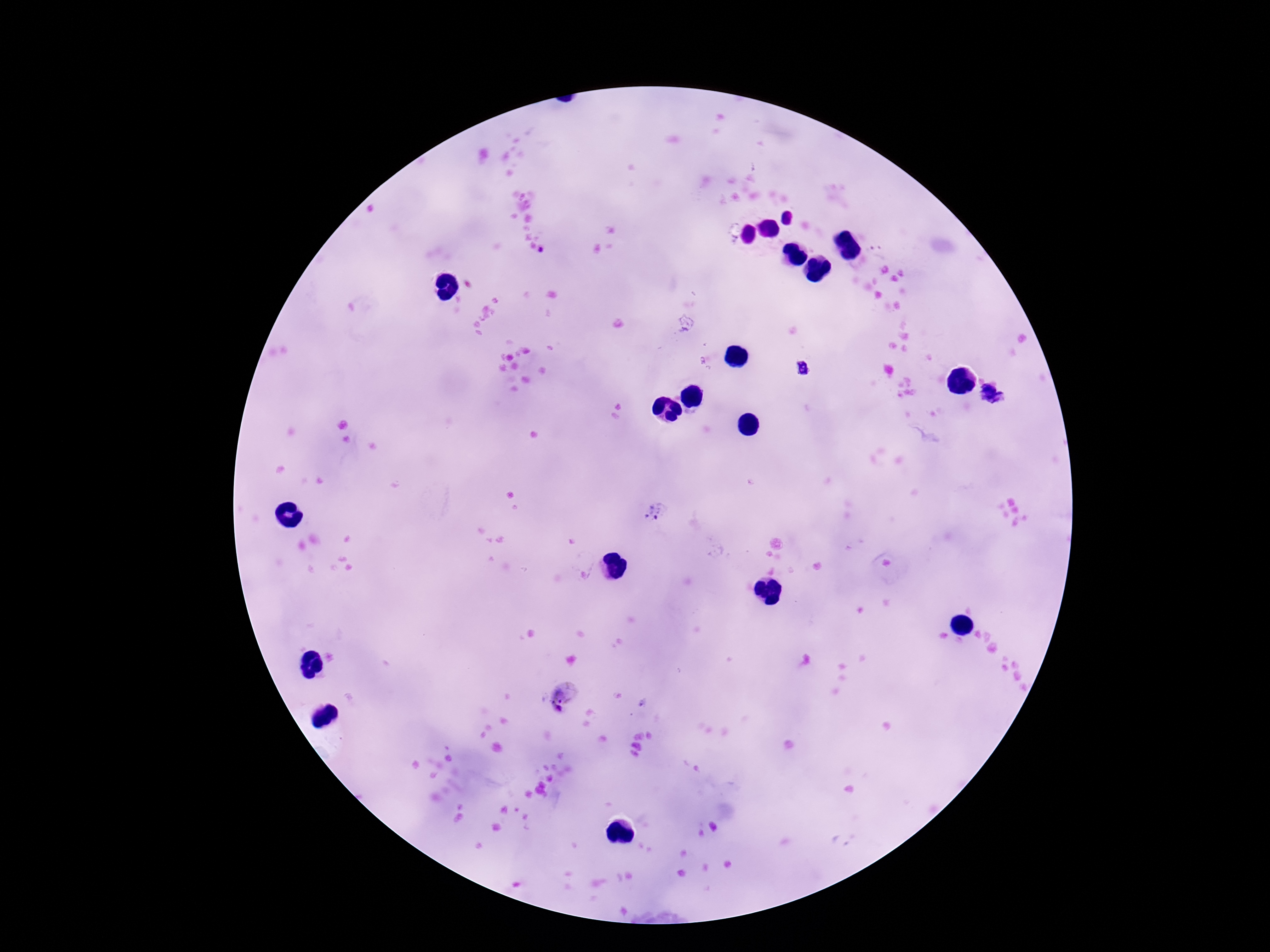
Approximate centers as {x, y} in pixels. Plasmodium parasite locations: {878, 249}, {804, 368}, {991, 397}, {654, 513}, {562, 698}. Thick blood smear. Image is 1270×952 pixels. 100x magnification. Smartphone photograph taken through the microscope eyepiece. Patient malaria status: infected. Single field of view. Giemsa stain.